Identify the parasite.
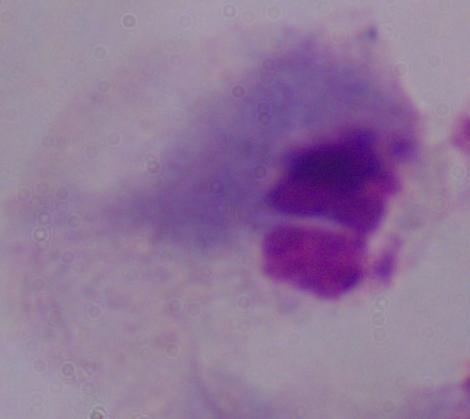
A trichomonad.

Summary:
  - Modality: photomicrograph
  - Magnification: 1000x